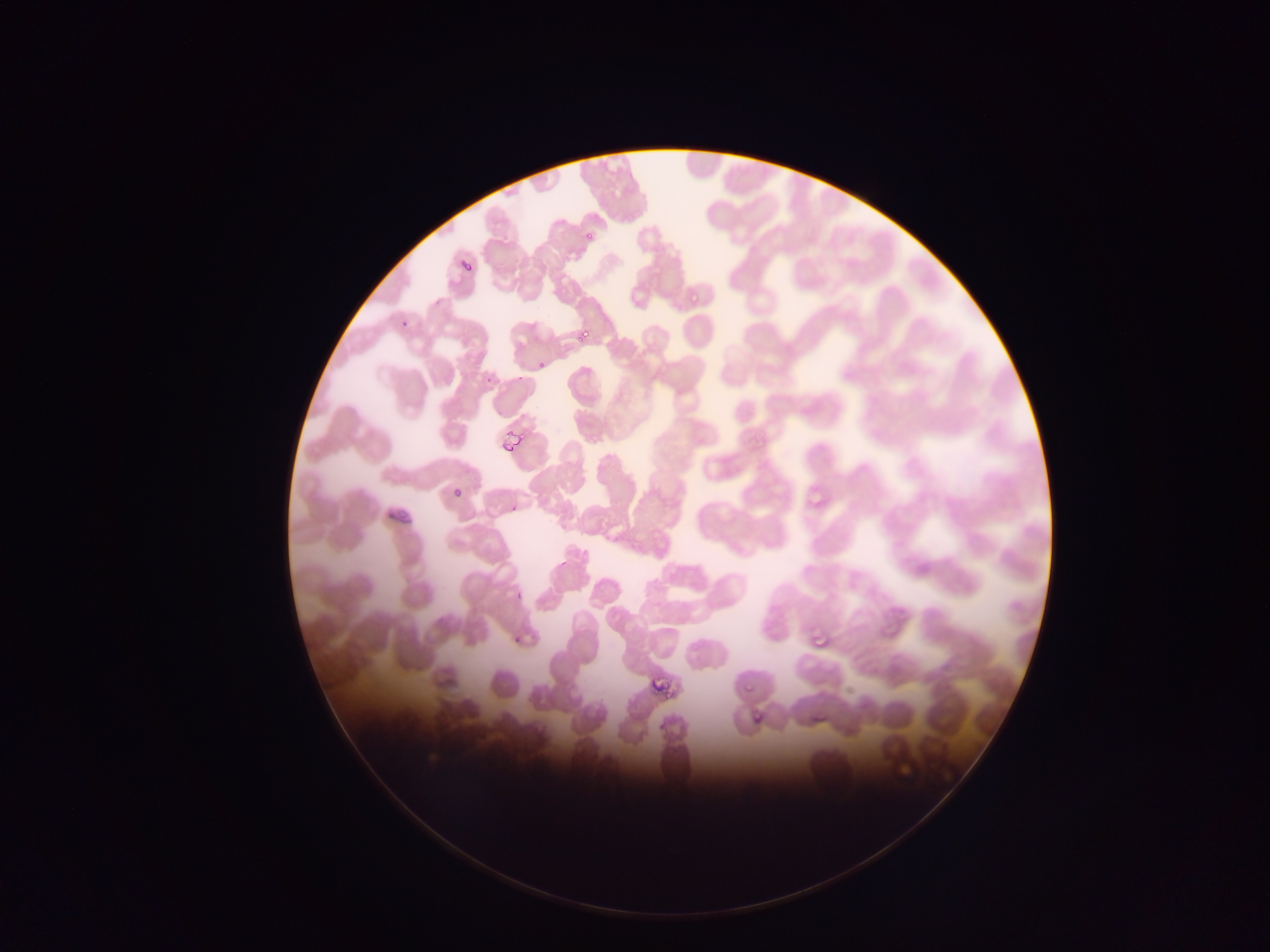
Approximate bounding boxes as {left, top, right, bottom} in pixels.
Summary:
  - Malaria parasite locations: {581, 227, 598, 244}, {460, 258, 475, 274}, {687, 290, 703, 301}, {399, 308, 414, 326}, {574, 328, 591, 341}, {539, 354, 553, 370}, {486, 359, 503, 384}, {509, 427, 522, 446}, {498, 439, 510, 457}, {446, 472, 469, 506}, {805, 487, 824, 504}, {503, 495, 526, 515}, {811, 624, 839, 652}, {647, 664, 679, 698}, {739, 673, 758, 692}, {808, 704, 831, 725}, {752, 713, 765, 722}
  - Image size: 1270×952 pixels
  - Capture: mobile-phone photograph through a microscope
  - Field of view: single
  - Country: Ghana
  - Preparation: thin blood smear